Identify the parasite.
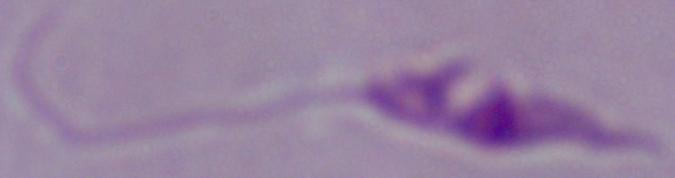
This is Leishmania.

Summary:
  - Magnification: 1000x
  - Modality: photomicrograph